Name the blood parasite species.
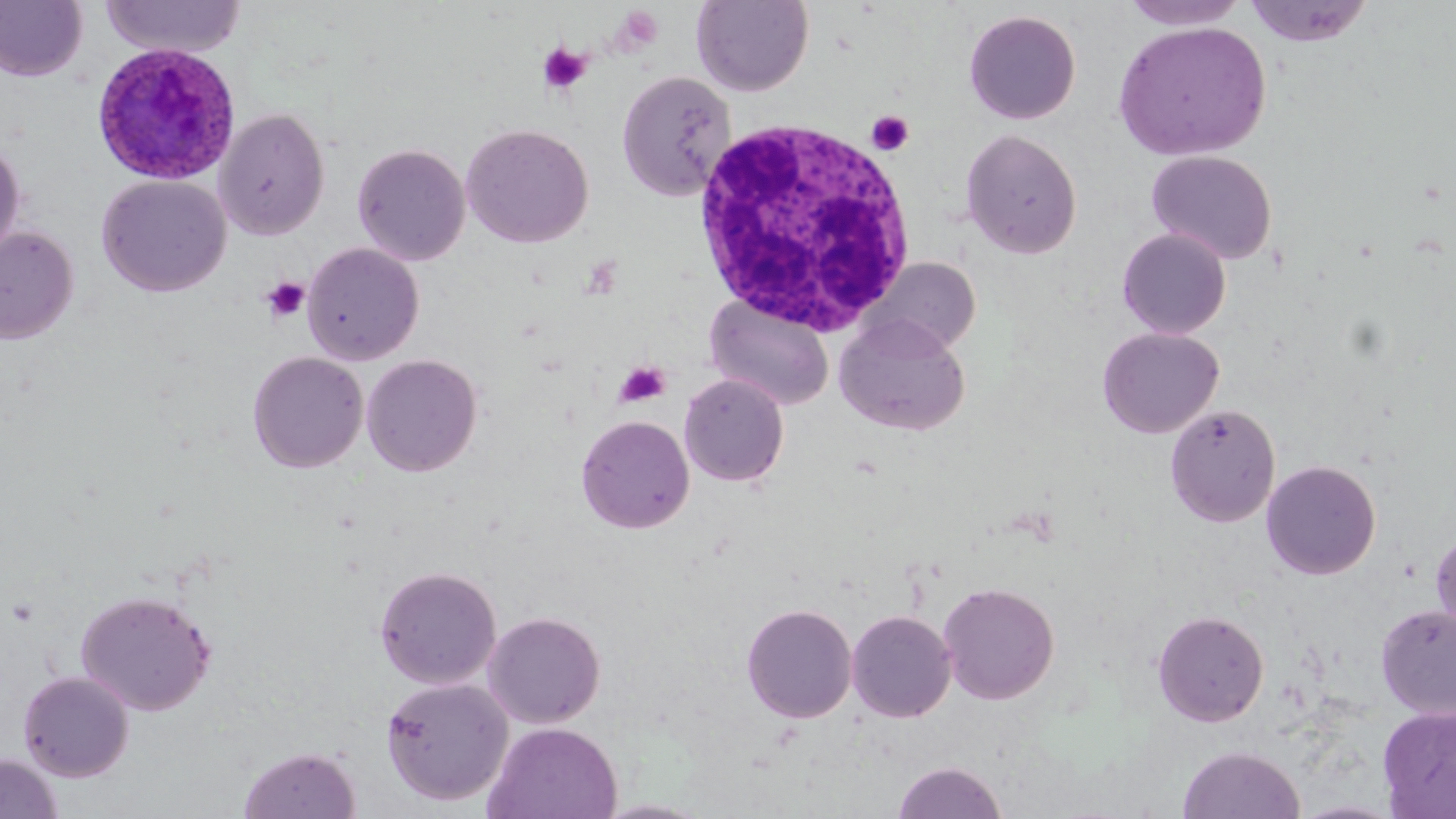

Plasmodium ovale.

preparation = thin blood film
image size = 1456×819 pixels
modality = optical microscopy
platelet locations = approximate bounding boxes as (x1, y1, x2, y2) in pixels: (537, 43, 591, 95), (866, 110, 914, 156), (261, 277, 310, 324), (615, 360, 670, 407)
magnification = 1000x
white blood cell locations = approximate bounding boxes as (x1, y1, x2, y2) in pixels: (689, 120, 918, 335)
uninfected red blood cell locations = approximate bounding boxes as (x1, y1, x2, y2) in pixels: (101, 0, 246, 59), (691, 0, 814, 96), (1119, 0, 1251, 30), (1243, 0, 1374, 47), (0, 1, 89, 82), (964, 9, 1082, 125), (1113, 21, 1271, 161), (616, 70, 737, 200), (214, 107, 330, 240), (461, 123, 594, 248), (961, 128, 1083, 259), (0, 136, 26, 261), (352, 143, 471, 265), (1146, 150, 1277, 264), (97, 175, 231, 297), (0, 226, 79, 344), (1117, 228, 1231, 339), (302, 243, 424, 365), (871, 257, 981, 355), (705, 295, 834, 411), (834, 314, 970, 435), (1097, 327, 1224, 438), (247, 351, 368, 473), (361, 354, 483, 477), (679, 373, 790, 487), (1165, 404, 1281, 527), (576, 414, 695, 534), (1261, 460, 1381, 580), (1430, 528, 1456, 643), (374, 565, 502, 689), (938, 581, 1059, 704), (75, 589, 216, 716), (741, 603, 858, 723), (1375, 604, 1456, 720), (846, 609, 957, 723), (1152, 610, 1269, 726), (482, 611, 606, 728), (18, 670, 135, 781), (381, 677, 514, 806), (1377, 705, 1456, 818), (483, 721, 623, 819), (238, 745, 360, 819), (1177, 745, 1305, 819), (0, 753, 63, 818), (891, 761, 1009, 819), (1289, 799, 1406, 818), (592, 800, 715, 818)
Plasmodium ovale-infected red blood cell locations = approximate bounding boxes as (x1, y1, x2, y2) in pixels: (92, 41, 241, 185)
stain = May-Grünwald-Giemsa
field of view = single